Name the blood parasite species.
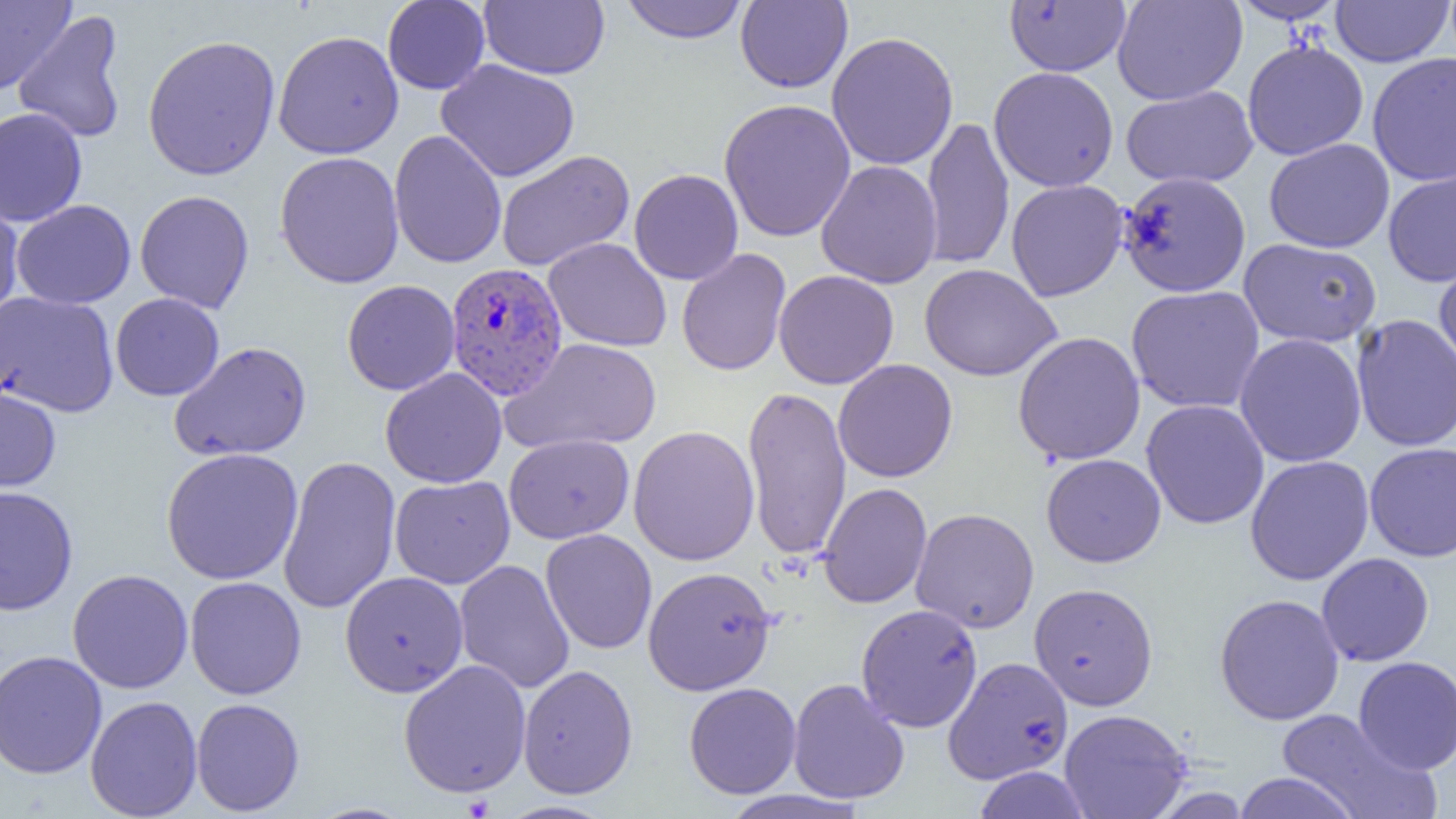
Plasmodium vivax.

Approximate bounding boxes as (x1, y1, x2, y2) in pixels. Plasmodium vivax-infected red blood cell locations: (444, 260, 568, 405). Uninfected red blood cell locations: (1, 0, 75, 95), (382, 0, 490, 95), (478, 0, 610, 79), (619, 0, 749, 44), (735, 0, 853, 93), (1112, 0, 1246, 105), (1229, 0, 1347, 24), (1331, 0, 1453, 67), (1004, 1, 1131, 76), (13, 11, 128, 144), (272, 30, 404, 159), (826, 31, 959, 171), (142, 34, 281, 181), (1242, 39, 1369, 160), (1367, 52, 1456, 187), (436, 59, 580, 182), (988, 66, 1119, 193), (1121, 85, 1258, 188), (718, 98, 856, 243), (0, 107, 88, 227), (921, 116, 1014, 271), (389, 129, 507, 269), (1264, 138, 1395, 253), (496, 150, 634, 271), (274, 151, 405, 289), (816, 160, 943, 288), (629, 169, 744, 285), (1382, 169, 1456, 287), (1117, 171, 1251, 297), (1006, 179, 1128, 301), (135, 190, 254, 313), (0, 194, 24, 322), (11, 200, 136, 309), (543, 237, 673, 352), (1238, 238, 1382, 348), (676, 248, 792, 377), (1434, 253, 1456, 375), (919, 263, 1061, 381), (773, 269, 899, 390), (342, 279, 460, 395), (1126, 285, 1265, 414), (0, 291, 119, 417), (110, 293, 225, 401), (1352, 314, 1456, 452), (1012, 331, 1146, 465), (1234, 333, 1367, 467), (501, 338, 661, 454), (169, 342, 312, 462), (832, 359, 958, 483), (380, 368, 507, 488), (0, 382, 62, 493), (742, 385, 852, 561), (1141, 399, 1270, 529), (628, 425, 760, 566), (504, 434, 634, 543), (1364, 442, 1456, 562), (161, 447, 303, 585), (1041, 453, 1166, 568), (277, 455, 401, 614), (1245, 455, 1374, 585), (390, 475, 515, 589), (818, 482, 933, 609), (0, 485, 78, 615), (910, 508, 1039, 633), (540, 528, 657, 655), (1316, 552, 1434, 667), (454, 559, 575, 694), (642, 566, 776, 695), (67, 569, 194, 693), (340, 571, 468, 697), (185, 576, 306, 700), (1029, 582, 1158, 710), (1214, 593, 1344, 725), (856, 603, 983, 732), (0, 650, 107, 779), (1353, 656, 1456, 774), (945, 657, 1072, 786), (398, 659, 532, 798), (518, 664, 638, 800), (787, 678, 910, 805), (684, 682, 801, 799), (85, 695, 203, 819), (190, 697, 305, 816), (1059, 709, 1192, 819), (1275, 709, 1440, 819), (971, 766, 1094, 819), (1231, 772, 1362, 819), (716, 789, 870, 819), (493, 800, 617, 819). One field of a larger specimen. Thin blood film. Image is 1456×819 pixels. Captured at 1000x magnification. Light microscopy.